Describe the morphology of the red blood cells.
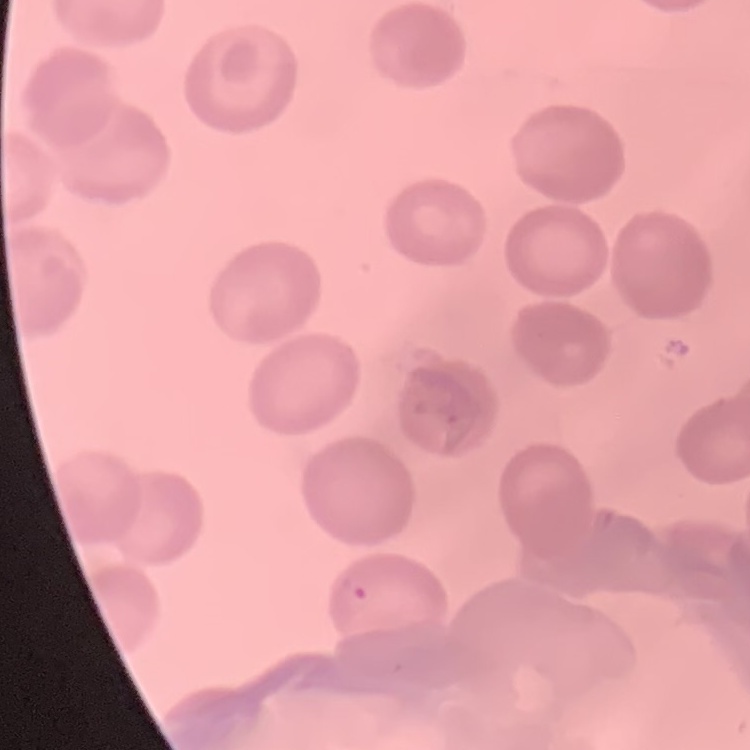

No rouleaux formation.

Stained with either Field's or Giemsa. Square crop of a larger photomicrograph. Thin peripheral smear.